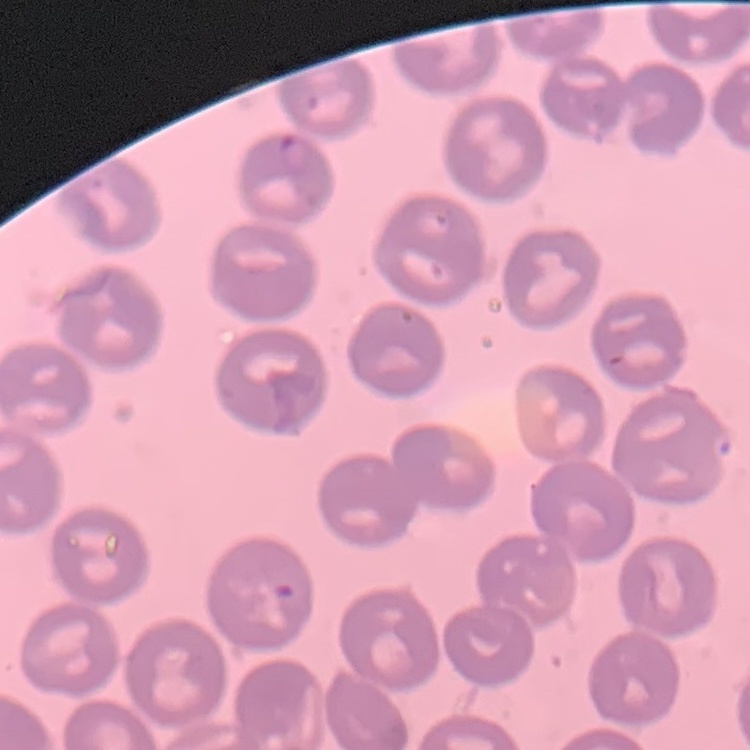
erythrocyte morphology = no rouleaux formation
image type = one tile cut from a larger photomicrograph
stain = Field's or Giemsa
preparation = thin blood film